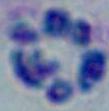
{
  "modality": "photomicrograph",
  "identification": "white blood cell",
  "magnification": "1000x"
}